Name the cell type shown.
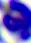

A leukocyte.

magnification: 400x
modality: micrograph